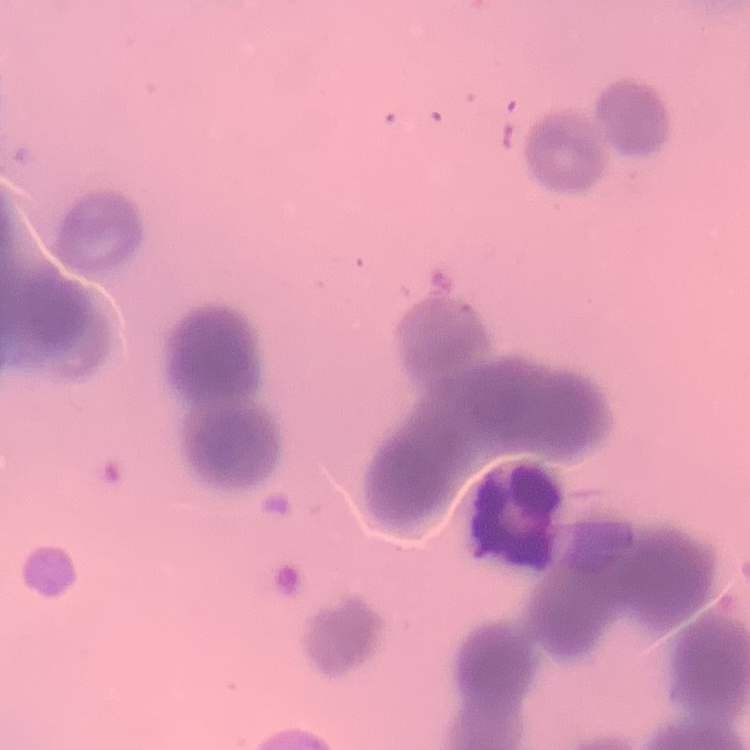
erythrocyte morphology = rouleaux formation
stain = Field's or Giemsa
preparation = thin blood smear
image type = one tile cut from a larger photomicrograph